Report the malaria status of this cell.
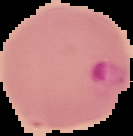

Parasitized.

Summary:
  - Preparation: thin blood smear
  - Image type: cell region segmented out of the field of view; surrounding area masked to black
  - Image size: 133×136 pixels